Assess this cell for malaria.
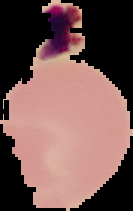

It is uninfected.

preparation: thin blood smear
image_type: cell region segmented out of the field of view; surrounding area masked to black
image_size: 133×211 pixels